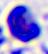 A leukocyte is shown. Captured at 400x magnification. Photomicrograph.